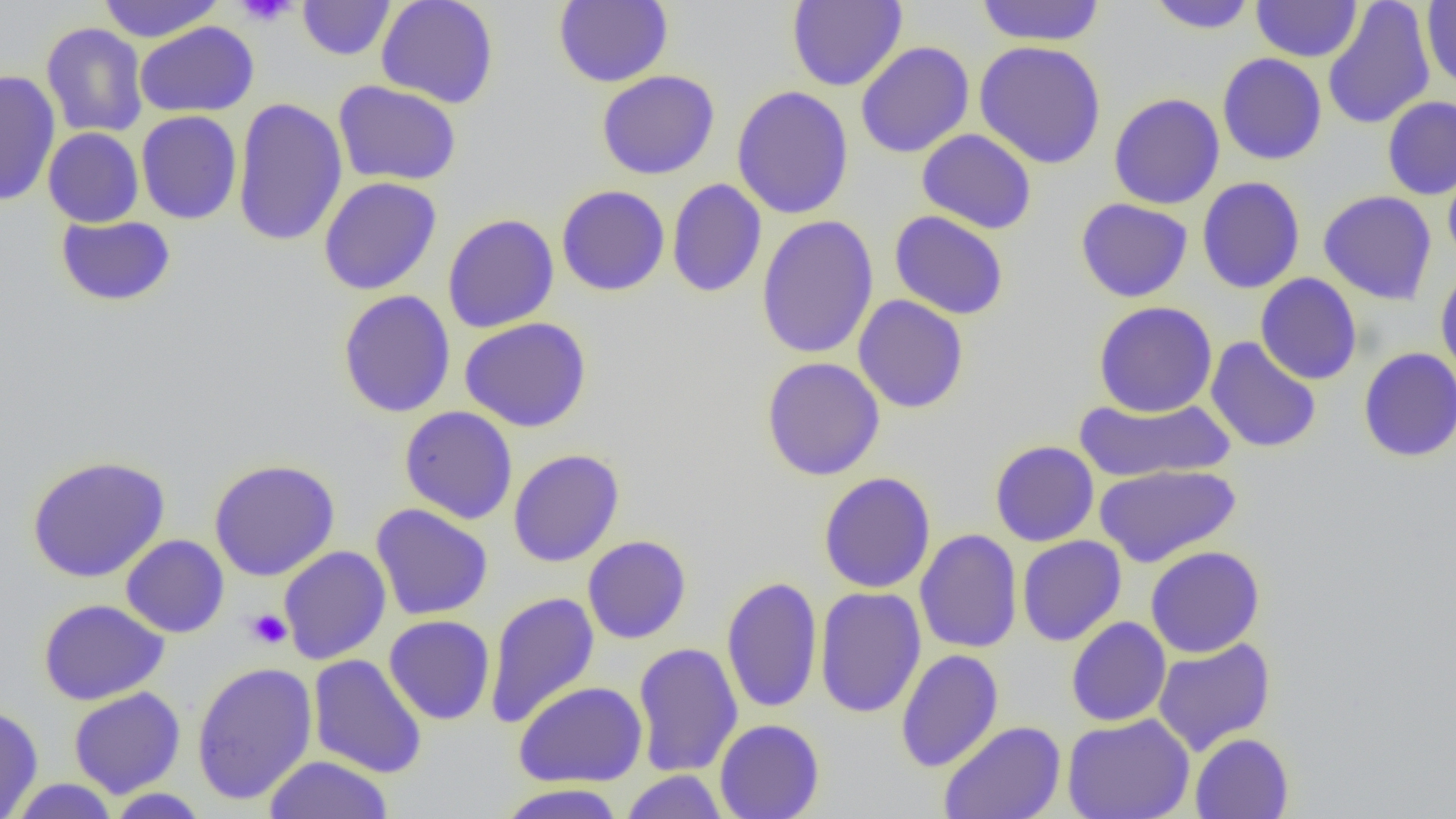
Approximate bounding boxes as (x1, y1, x2, y2) in pixels. Platelet locations: (234, 0, 299, 26), (245, 609, 292, 649). Uninfected red blood cell locations: (96, 0, 225, 42), (376, 0, 499, 109), (553, 0, 673, 88), (787, 0, 907, 91), (975, 0, 1106, 47), (1145, 0, 1259, 34), (297, 1, 396, 60), (1252, 1, 1362, 62), (1322, 1, 1436, 130), (1422, 1, 1455, 89), (135, 21, 259, 118), (41, 22, 148, 138), (974, 40, 1107, 169), (855, 41, 974, 158), (1217, 53, 1327, 165), (0, 70, 61, 208), (596, 70, 720, 180), (333, 80, 462, 186), (732, 86, 854, 219), (1108, 93, 1224, 210), (1382, 96, 1456, 200), (232, 97, 348, 247), (136, 110, 242, 225), (43, 127, 144, 227), (917, 128, 1037, 234), (1443, 162, 1456, 268), (1197, 176, 1305, 294), (318, 177, 442, 295), (667, 178, 767, 298), (556, 185, 670, 297), (1318, 190, 1437, 305), (1075, 198, 1193, 303), (889, 210, 1009, 320), (442, 214, 559, 333), (55, 215, 176, 307), (756, 215, 879, 359), (1435, 267, 1456, 381), (1255, 273, 1363, 385), (337, 290, 456, 418), (853, 295, 969, 413), (1093, 301, 1218, 417), (460, 317, 592, 433), (1205, 337, 1321, 454), (1358, 347, 1456, 462), (761, 356, 886, 481), (1073, 395, 1235, 483), (399, 406, 518, 524), (990, 440, 1099, 546), (507, 448, 624, 567), (26, 454, 171, 583), (209, 458, 341, 581), (1093, 464, 1242, 567), (818, 471, 936, 594), (371, 503, 494, 621), (915, 529, 1022, 653), (121, 534, 229, 638), (582, 535, 692, 644), (1017, 535, 1126, 646), (279, 545, 391, 664), (1145, 545, 1265, 657), (721, 575, 823, 714), (814, 587, 927, 718), (484, 591, 599, 730), (38, 599, 170, 705), (384, 615, 495, 725), (1066, 616, 1171, 727), (1152, 637, 1276, 756), (632, 642, 743, 777), (896, 649, 1004, 771), (308, 654, 427, 779), (191, 662, 318, 805), (514, 681, 648, 787), (68, 687, 186, 798), (0, 705, 43, 818), (1061, 713, 1195, 819), (714, 719, 825, 819), (938, 721, 1066, 819), (1190, 732, 1294, 819), (263, 755, 394, 818), (620, 770, 729, 819), (8, 778, 121, 818), (495, 783, 626, 818), (103, 788, 211, 818). Slide-level diagnosis: negative for blood parasites. Captured at 1000x magnification. Thin blood smear. Light microscopy. One field of a larger specimen. Image is 1456×819 pixels.